Assess the morphology of the red blood cells.
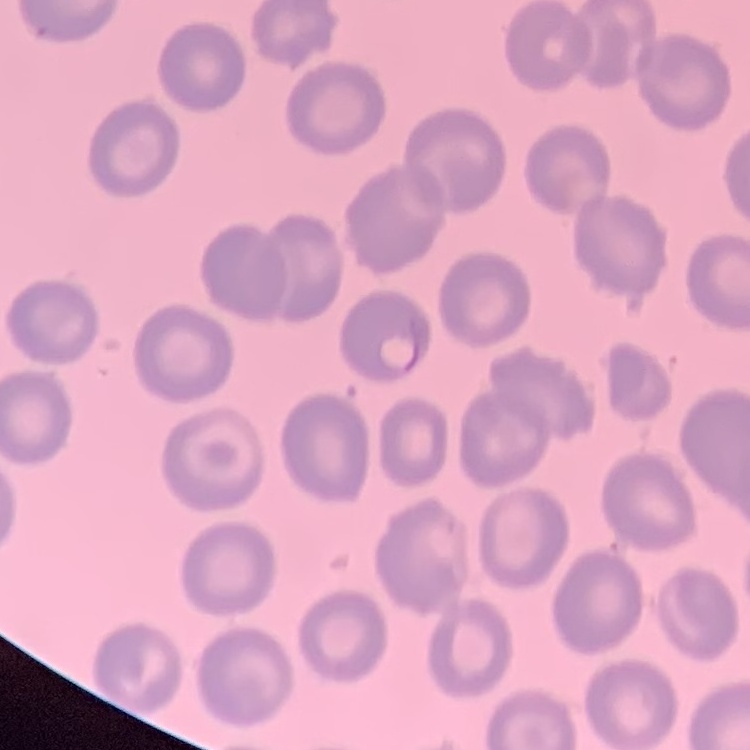

No rouleaux formation.

Summary:
  - Stain: Field's or Giemsa
  - Image type: one tile cut from a larger photomicrograph
  - Preparation: thin blood film